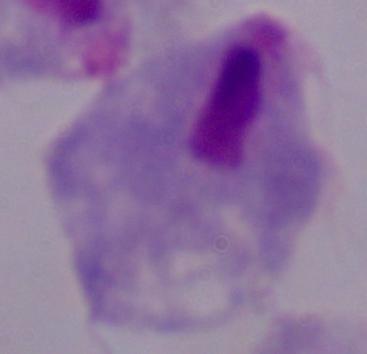

magnification = 1000x
modality = micrograph
identification = trichomonad